Assess this cell for malaria.
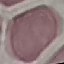
Uninfected.

{
  "preparation": "thin blood film",
  "stain": "Giemsa",
  "capture": "smartphone through the microscope eyepiece",
  "image_type": "automatically extracted cell patch, resized to 64 × 64 pixels"
}